Report the malaria status of this cell.
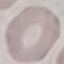
It is uninfected.

Summary:
  - Stain: Giemsa
  - Preparation: thin blood smear
  - Image type: cell patch, automatically extracted from a larger field of view and resized to 64 × 64 pixels
  - Capture: smartphone through the microscope eyepiece